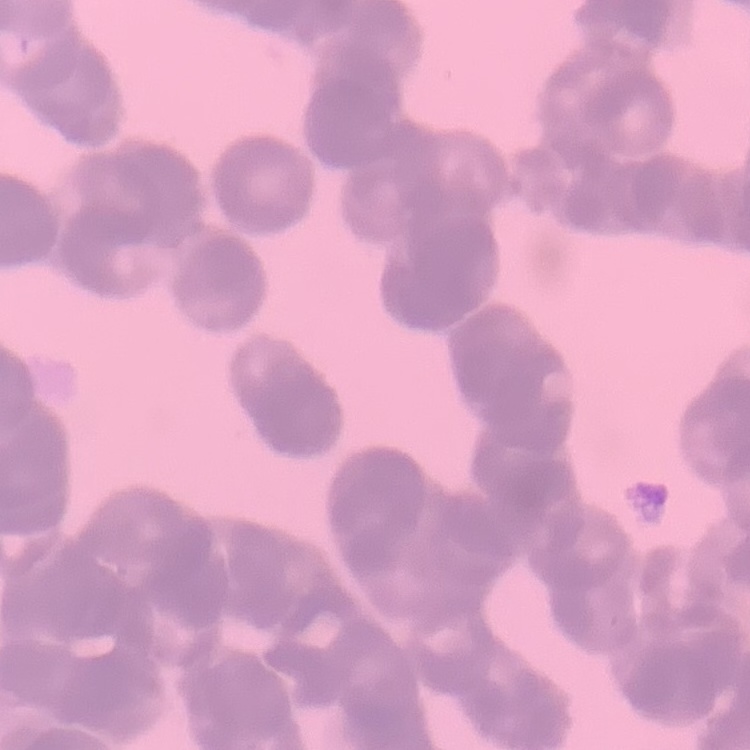 The erythrocytes exhibit rouleaux formation. One tile cut from a larger photomicrograph. Stained with either Field's or Giemsa. Thin peripheral smear.